Assess this cell for malaria.
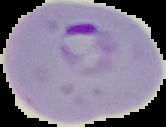
It is parasitized.

Image is 166×127 pixels. From a thin blood smear. Cell region segmented out of the field of view; the surrounding area is masked to black.